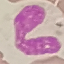 Result: no malaria parasites seen. Cell patch, automatically extracted from a larger field of view and resized to 64 × 64 pixels. Thin blood film. Photographed with a smartphone camera at the microscope eyepiece. Giemsa stain.